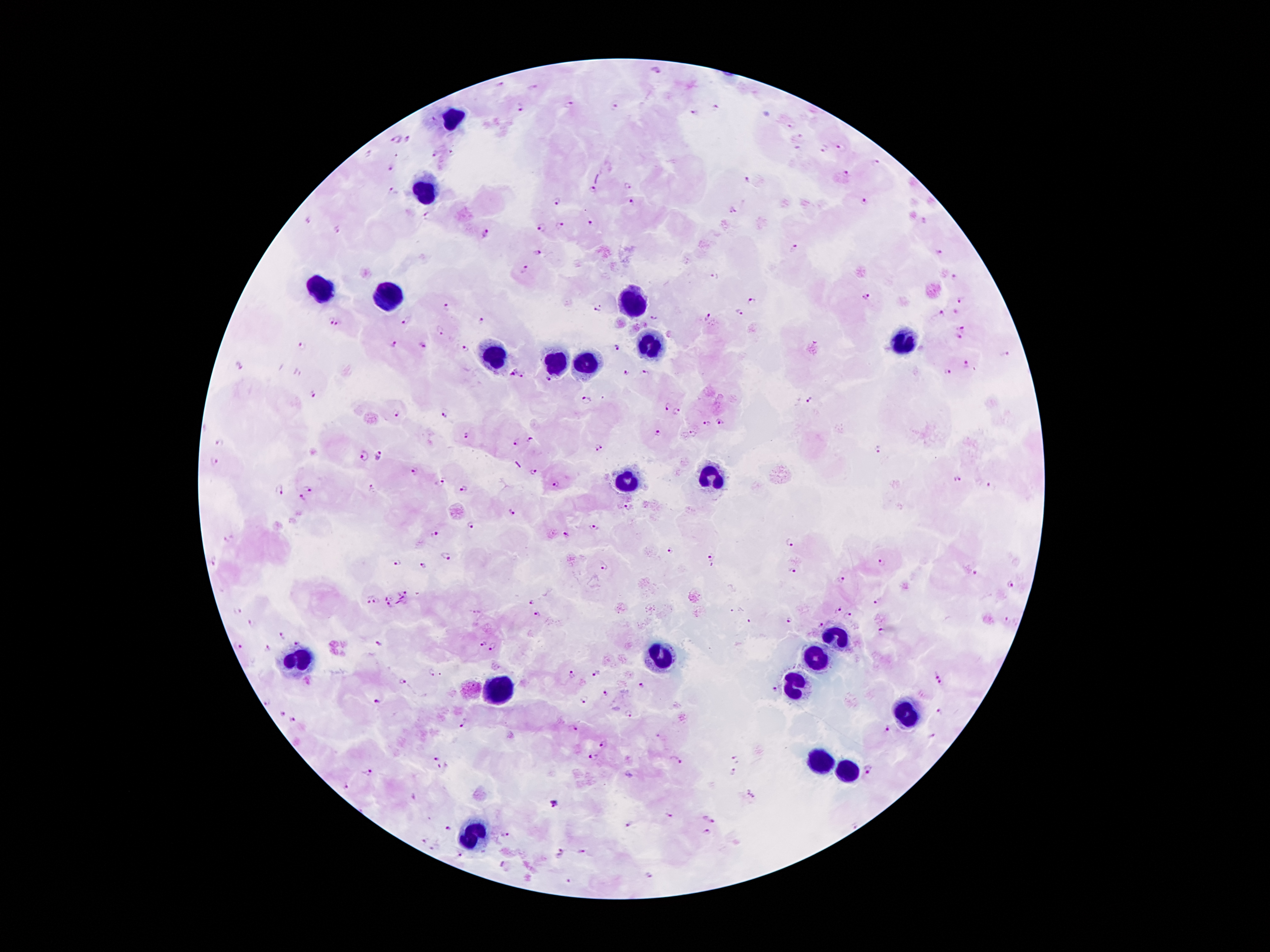

Patient malaria status: infected with Plasmodium falciparum. Giemsa-stained preparation. Image is 1270×952 pixels. 100x magnification. One field from this slide. Thick peripheral-blood smear. Photographed through the microscope eyepiece with a smartphone camera.